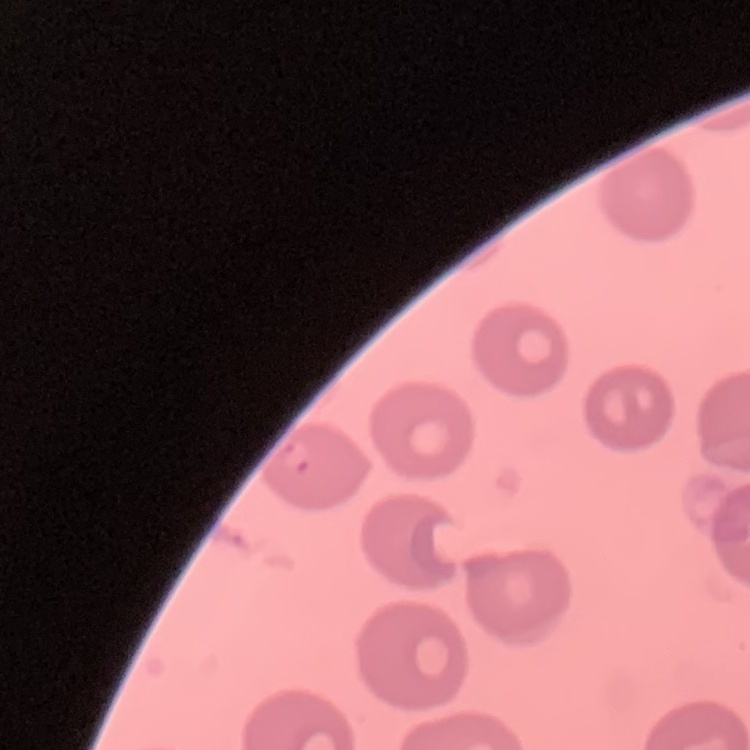
The red blood cells show no rouleaux formation. Square crop of a larger photomicrograph. Thin blood smear. Field's or Giemsa stain.